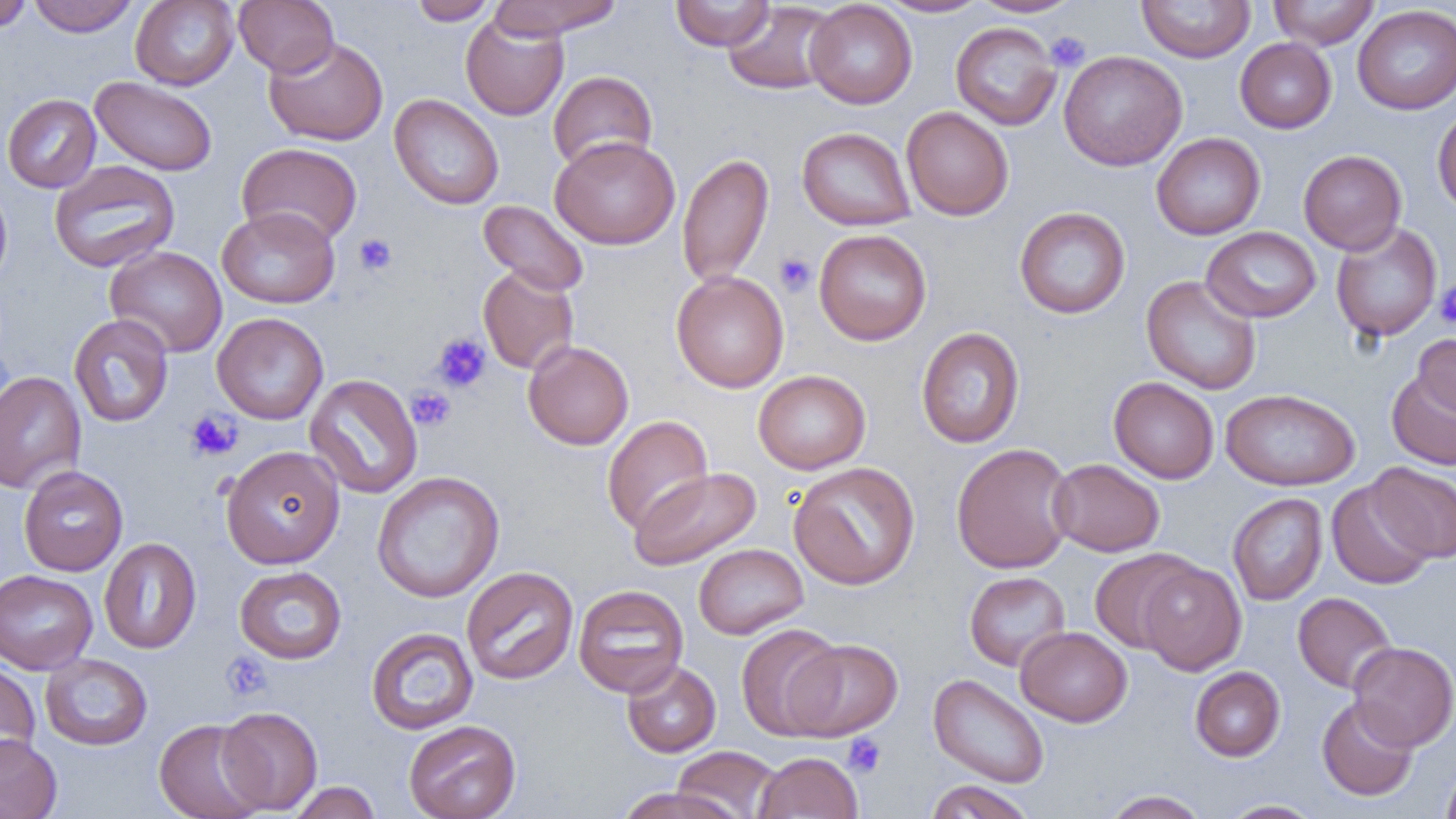
Summary:
  - Coordinate format: approximate bounding boxes as named x1/y1/x2/y2 corners in pixels
  - Platelet locations: (x1=1046, y1=31, x2=1090, y2=71), (x1=354, y1=233, x2=397, y2=276), (x1=774, y1=252, x2=817, y2=296), (x1=1434, y1=281, x2=1456, y2=330), (x1=432, y1=332, x2=492, y2=393), (x1=407, y1=386, x2=455, y2=431), (x1=185, y1=409, x2=243, y2=462), (x1=220, y1=651, x2=274, y2=702), (x1=842, y1=733, x2=886, y2=777)
  - Uninfected red blood cell locations: (x1=0, y1=0, x2=33, y2=33), (x1=28, y1=0, x2=139, y2=37), (x1=130, y1=0, x2=239, y2=90), (x1=234, y1=0, x2=338, y2=77), (x1=409, y1=0, x2=497, y2=25), (x1=488, y1=0, x2=624, y2=39), (x1=670, y1=0, x2=775, y2=52), (x1=876, y1=0, x2=991, y2=17), (x1=969, y1=0, x2=1083, y2=17), (x1=1137, y1=0, x2=1255, y2=62), (x1=1268, y1=0, x2=1379, y2=49), (x1=805, y1=1, x2=917, y2=109), (x1=722, y1=2, x2=839, y2=95), (x1=1353, y1=5, x2=1456, y2=114), (x1=460, y1=13, x2=569, y2=121), (x1=950, y1=22, x2=1061, y2=130), (x1=263, y1=35, x2=388, y2=146), (x1=1235, y1=37, x2=1336, y2=133), (x1=1059, y1=50, x2=1187, y2=171), (x1=548, y1=70, x2=658, y2=173), (x1=90, y1=76, x2=217, y2=176), (x1=2, y1=93, x2=101, y2=193), (x1=389, y1=94, x2=504, y2=209), (x1=1432, y1=105, x2=1456, y2=216), (x1=901, y1=106, x2=1014, y2=221), (x1=797, y1=127, x2=915, y2=230), (x1=1152, y1=132, x2=1266, y2=240), (x1=550, y1=135, x2=680, y2=250), (x1=236, y1=142, x2=362, y2=247), (x1=1298, y1=149, x2=1407, y2=255), (x1=677, y1=152, x2=774, y2=288), (x1=49, y1=160, x2=180, y2=273), (x1=0, y1=180, x2=13, y2=290), (x1=478, y1=199, x2=589, y2=296), (x1=216, y1=206, x2=341, y2=308), (x1=1014, y1=207, x2=1130, y2=318), (x1=1331, y1=222, x2=1442, y2=342), (x1=1201, y1=226, x2=1321, y2=323), (x1=813, y1=228, x2=931, y2=345), (x1=105, y1=246, x2=227, y2=357), (x1=478, y1=264, x2=579, y2=375), (x1=671, y1=270, x2=789, y2=393), (x1=1142, y1=275, x2=1262, y2=395), (x1=212, y1=312, x2=328, y2=425), (x1=69, y1=314, x2=174, y2=427), (x1=915, y1=326, x2=1025, y2=448), (x1=1414, y1=333, x2=1456, y2=420), (x1=523, y1=340, x2=634, y2=450), (x1=753, y1=369, x2=871, y2=474), (x1=1386, y1=369, x2=1456, y2=470), (x1=0, y1=370, x2=86, y2=495), (x1=304, y1=373, x2=423, y2=499), (x1=1108, y1=377, x2=1220, y2=484), (x1=1220, y1=388, x2=1360, y2=491), (x1=602, y1=415, x2=713, y2=534), (x1=951, y1=442, x2=1075, y2=574), (x1=221, y1=444, x2=345, y2=569), (x1=1049, y1=458, x2=1164, y2=556), (x1=788, y1=461, x2=920, y2=590), (x1=1368, y1=462, x2=1456, y2=563), (x1=18, y1=465, x2=128, y2=576), (x1=629, y1=467, x2=761, y2=570), (x1=372, y1=471, x2=505, y2=603), (x1=1326, y1=480, x2=1436, y2=590), (x1=1228, y1=492, x2=1328, y2=605), (x1=99, y1=537, x2=201, y2=654), (x1=694, y1=543, x2=809, y2=639), (x1=1090, y1=548, x2=1200, y2=654), (x1=1138, y1=561, x2=1246, y2=675), (x1=234, y1=566, x2=347, y2=664), (x1=461, y1=566, x2=579, y2=685), (x1=0, y1=569, x2=97, y2=675), (x1=965, y1=571, x2=1071, y2=671), (x1=573, y1=584, x2=689, y2=697), (x1=1293, y1=592, x2=1397, y2=693), (x1=736, y1=624, x2=845, y2=740), (x1=1016, y1=626, x2=1132, y2=727), (x1=365, y1=627, x2=479, y2=735), (x1=785, y1=638, x2=903, y2=740), (x1=1348, y1=641, x2=1456, y2=751), (x1=40, y1=653, x2=153, y2=750), (x1=621, y1=659, x2=721, y2=757), (x1=0, y1=661, x2=41, y2=768), (x1=1190, y1=666, x2=1285, y2=761), (x1=928, y1=673, x2=1050, y2=788), (x1=1316, y1=696, x2=1419, y2=801), (x1=217, y1=706, x2=323, y2=814), (x1=154, y1=719, x2=266, y2=819), (x1=404, y1=719, x2=521, y2=819), (x1=0, y1=733, x2=62, y2=819), (x1=672, y1=746, x2=781, y2=818), (x1=753, y1=752, x2=863, y2=819), (x1=1441, y1=761, x2=1456, y2=819), (x1=925, y1=780, x2=1036, y2=819), (x1=289, y1=781, x2=382, y2=819), (x1=613, y1=786, x2=747, y2=819), (x1=1102, y1=790, x2=1210, y2=819), (x1=1219, y1=799, x2=1325, y2=818)
  - Slide-level diagnosis: no evidence of blood parasites
  - Image size: 1456×819 pixels
  - Preparation: thin blood smear
  - Modality: light microscopy
  - Magnification: 1000x
  - Field of view: one of a larger specimen